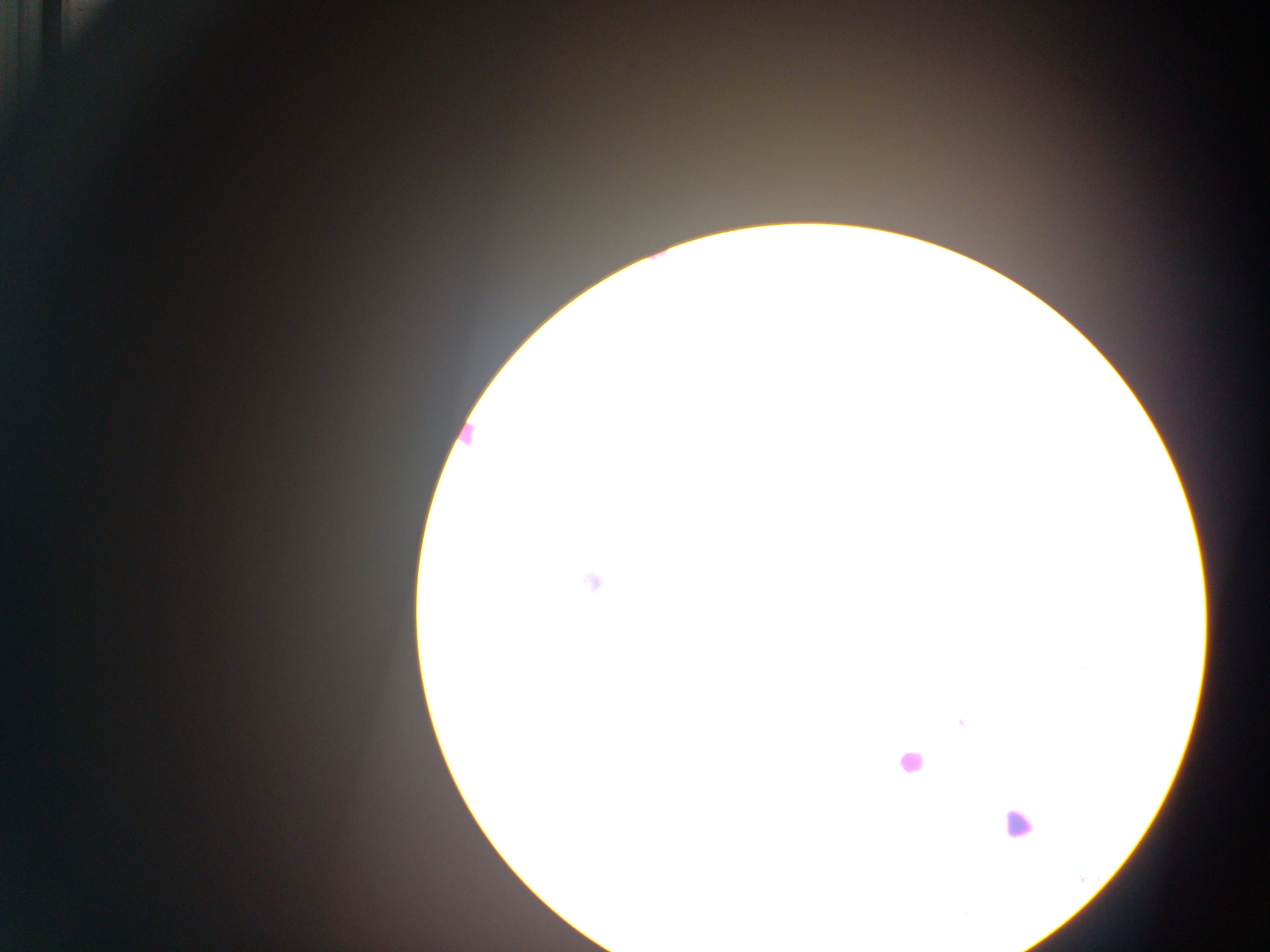

preparation = thick blood film
field of view = single
image size = 1270×952 pixels
country = Ghana
malaria parasite locations = approximate centers as [x, y] in pixels: [592, 582], [961, 722]
leukocyte locations = approximate centers as [x, y] in pixels: [465, 434], [909, 761], [1017, 824]
capture = mobile-phone photograph through a microscope